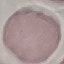

Result: no malaria parasites seen. Acquired by smartphone through the microscope eyepiece. Thin blood film. Giemsa stain. Automatically extracted cell patch, resized to 64 × 64 pixels.